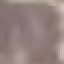

Malaria status: uninfected. Cell patch, automatically extracted from a larger field of view and resized to 64 × 64 pixels. Thin blood film. Photographed with a smartphone camera at the microscope eyepiece. Giemsa-stained preparation.